Outline each blood parasite and name the species.
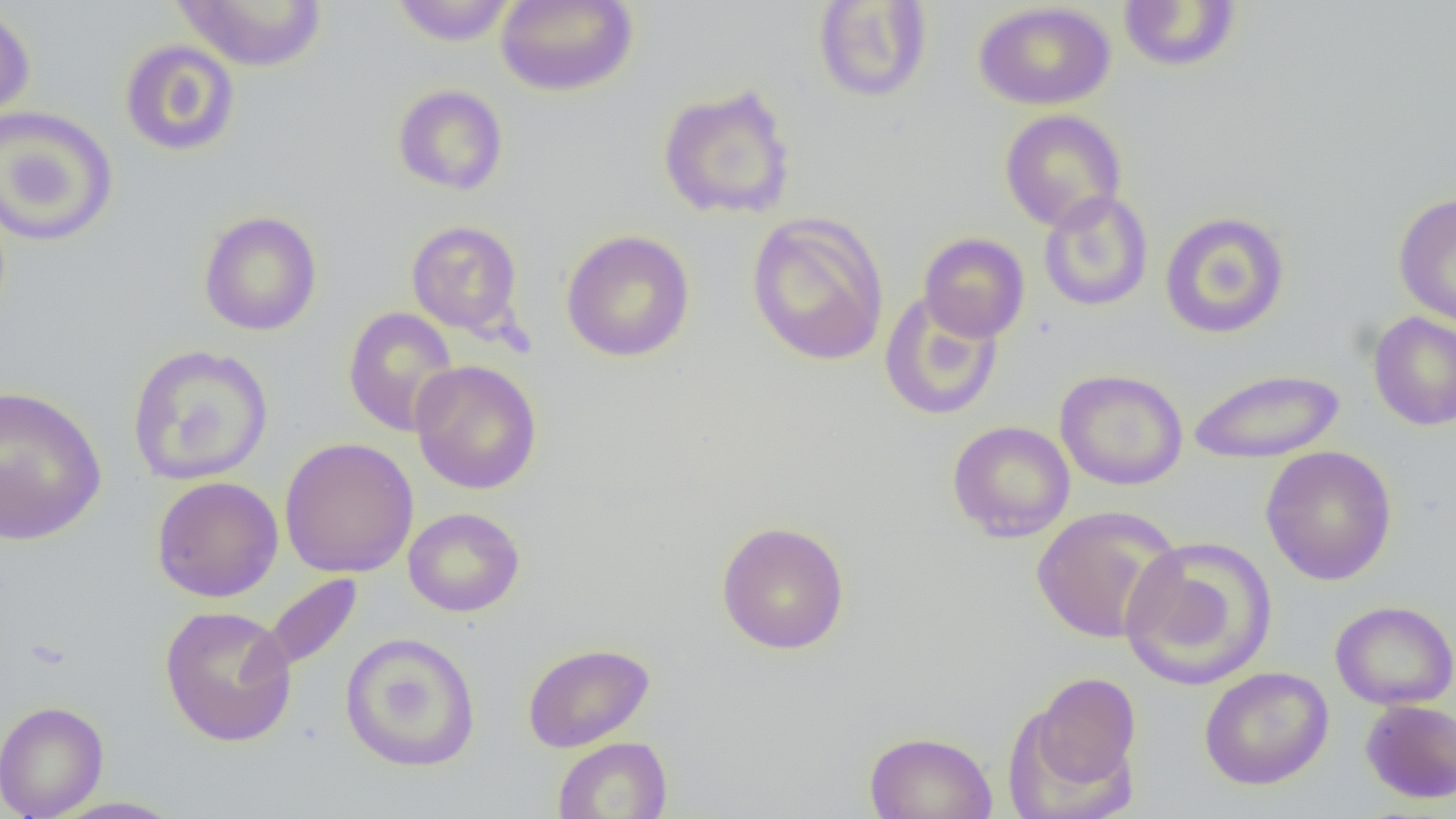

No blood parasites seen.

Summary:
  - Coordinate format: approximate bounding boxes as [x1, y1, x2, y2] in pixels
  - Uninfected red blood cell locations: [171, 0, 329, 72], [495, 0, 638, 97], [389, 1, 518, 45], [812, 1, 933, 103], [1117, 1, 1242, 74], [974, 2, 1115, 110], [0, 3, 36, 129], [119, 39, 241, 157], [656, 83, 797, 221], [392, 84, 509, 196], [0, 105, 118, 247], [999, 109, 1127, 231], [1038, 190, 1153, 312], [1393, 192, 1456, 328], [198, 210, 323, 337], [1159, 210, 1290, 339], [746, 211, 890, 367], [406, 220, 524, 337], [560, 229, 695, 362], [919, 232, 1030, 343], [879, 290, 1003, 421], [343, 306, 460, 437], [1368, 312, 1456, 431], [126, 343, 274, 485], [410, 359, 542, 494], [1187, 367, 1346, 465], [1055, 369, 1188, 490], [0, 385, 107, 547], [947, 420, 1076, 542], [279, 437, 419, 578], [1260, 445, 1398, 586], [151, 475, 284, 602], [1031, 505, 1183, 644], [403, 507, 525, 617], [715, 520, 851, 655], [1119, 536, 1278, 691], [261, 574, 362, 673], [1329, 600, 1456, 710], [159, 605, 298, 748], [340, 631, 481, 772], [522, 641, 654, 753], [1198, 666, 1334, 790], [1018, 670, 1142, 808], [1360, 699, 1456, 804], [0, 700, 109, 819], [863, 730, 998, 819], [552, 736, 673, 818], [46, 796, 187, 818]
  - Slide-level diagnosis: no evidence of blood parasites
  - Image size: 1456×819 pixels
  - Magnification: 1000x
  - Modality: light microscopy
  - Preparation: thin blood smear
  - Field of view: single